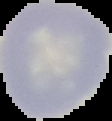

Summary:
  - Image type: cell region segmented out of the field of view; surrounding area masked to black
  - Preparation: thin blood film
  - Image size: 112×121 pixels
  - Malaria status: uninfected